Give the extent of all Plasmodium falciparum-infected red blood cells.
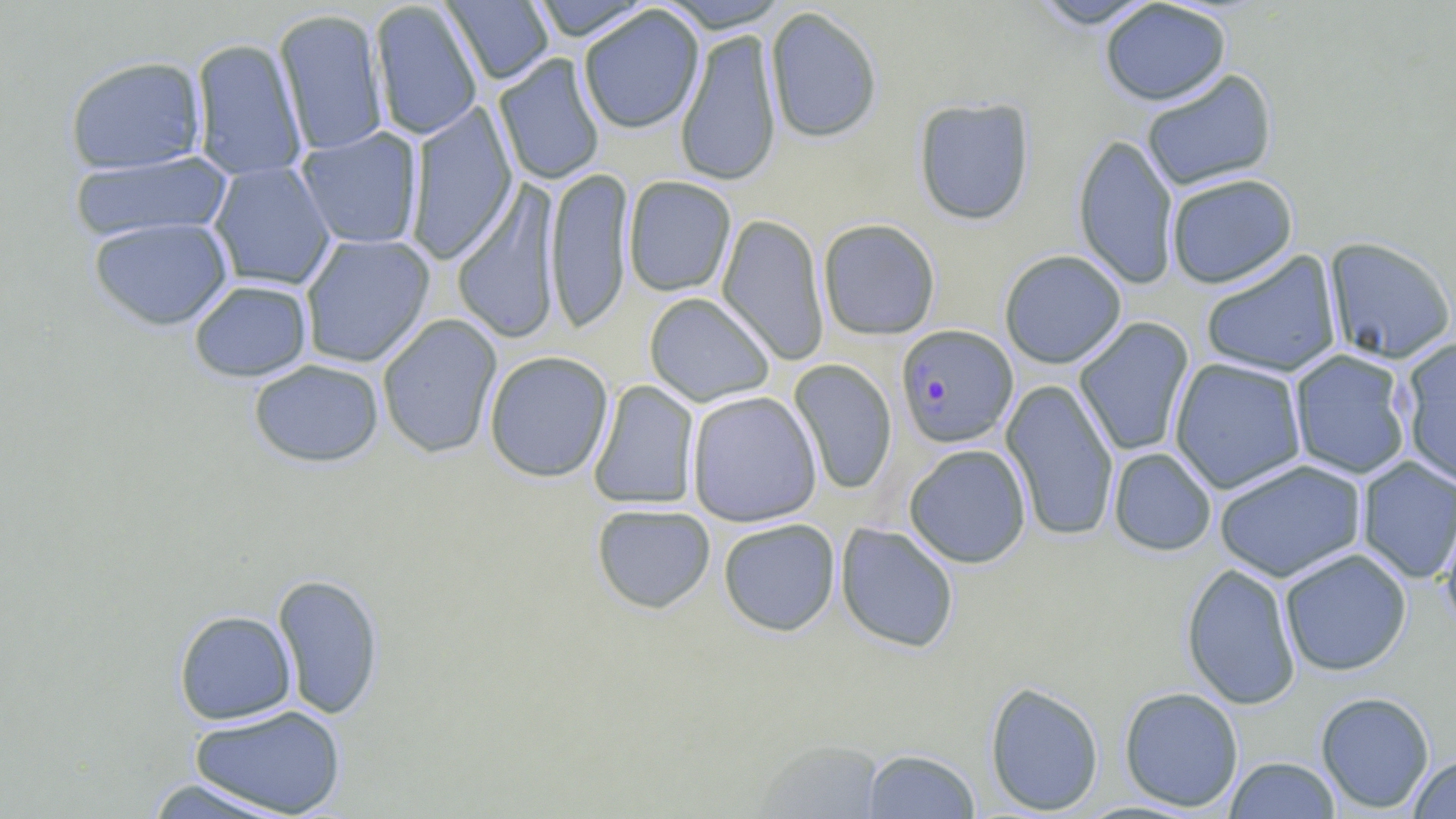

Approximate bounding boxes as (x1,y1)-(x2,y2) corner pairs in pixels.
Plasmodium falciparum-infected red blood cells: (896,325)-(1018,448).

{
  "slide_level_diagnosis": "Plasmodium falciparum",
  "preparation": "thin blood film",
  "uninfected_red_blood_cell_locations": "approximate bounding boxes as (x1,y1)-(x2,y2) corner pairs in pixels: (526,0)-(656,41), (657,0)-(790,32), (1025,0)-(1161,29), (369,1)-(483,140), (441,1)-(555,85), (1099,1)-(1231,106), (578,6)-(705,135), (764,6)-(883,143), (273,8)-(389,157), (675,27)-(783,187), (190,38)-(308,183), (493,53)-(606,186), (64,55)-(206,174), (1141,69)-(1278,192), (913,97)-(1035,225), (405,101)-(519,264), (295,127)-(424,249), (1072,132)-(1179,290), (69,151)-(233,243), (208,161)-(337,291), (545,166)-(633,334), (1166,173)-(1298,289), (623,176)-(737,297), (451,180)-(563,345), (716,213)-(830,366), (88,217)-(234,331), (817,218)-(941,341), (299,233)-(435,368), (1323,236)-(1456,364), (999,250)-(1127,369), (1200,250)-(1343,378), (188,279)-(313,382), (643,292)-(775,408), (376,313)-(503,460), (1073,317)-(1195,458), (1399,337)-(1456,490), (1288,349)-(1413,480), (484,350)-(614,483), (1169,358)-(1307,493), (248,359)-(384,468), (789,359)-(897,495), (588,379)-(701,510), (1001,379)-(1119,542), (686,390)-(822,527), (904,444)-(1032,568), (1108,448)-(1217,556), (1355,456)-(1455,584), (1213,458)-(1368,582), (591,504)-(716,614), (1439,505)-(1456,637), (718,518)-(840,636), (835,522)-(959,653), (1279,548)-(1412,676), (1181,562)-(1301,710), (272,573)-(385,721), (174,610)-(297,724), (985,681)-(1104,816), (1118,686)-(1244,811), (1315,692)-(1435,813), (188,705)-(346,817), (755,739)-(887,818), (862,748)-(981,818), (1407,753)-(1456,818), (1224,756)-(1341,818), (141,777)-(302,819)",
  "image_size": "1456×819 pixels",
  "modality": "optical microscopy",
  "stain": "May-Grünwald-Giemsa",
  "field_of_view": "one of a larger specimen",
  "magnification": "1000x"
}